Classify this cell by malaria status.
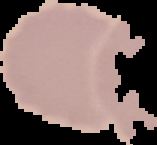
Uninfected.

Summary:
  - Image type: segmented cell region on a black background
  - Preparation: thin blood film
  - Image size: 157×145 pixels